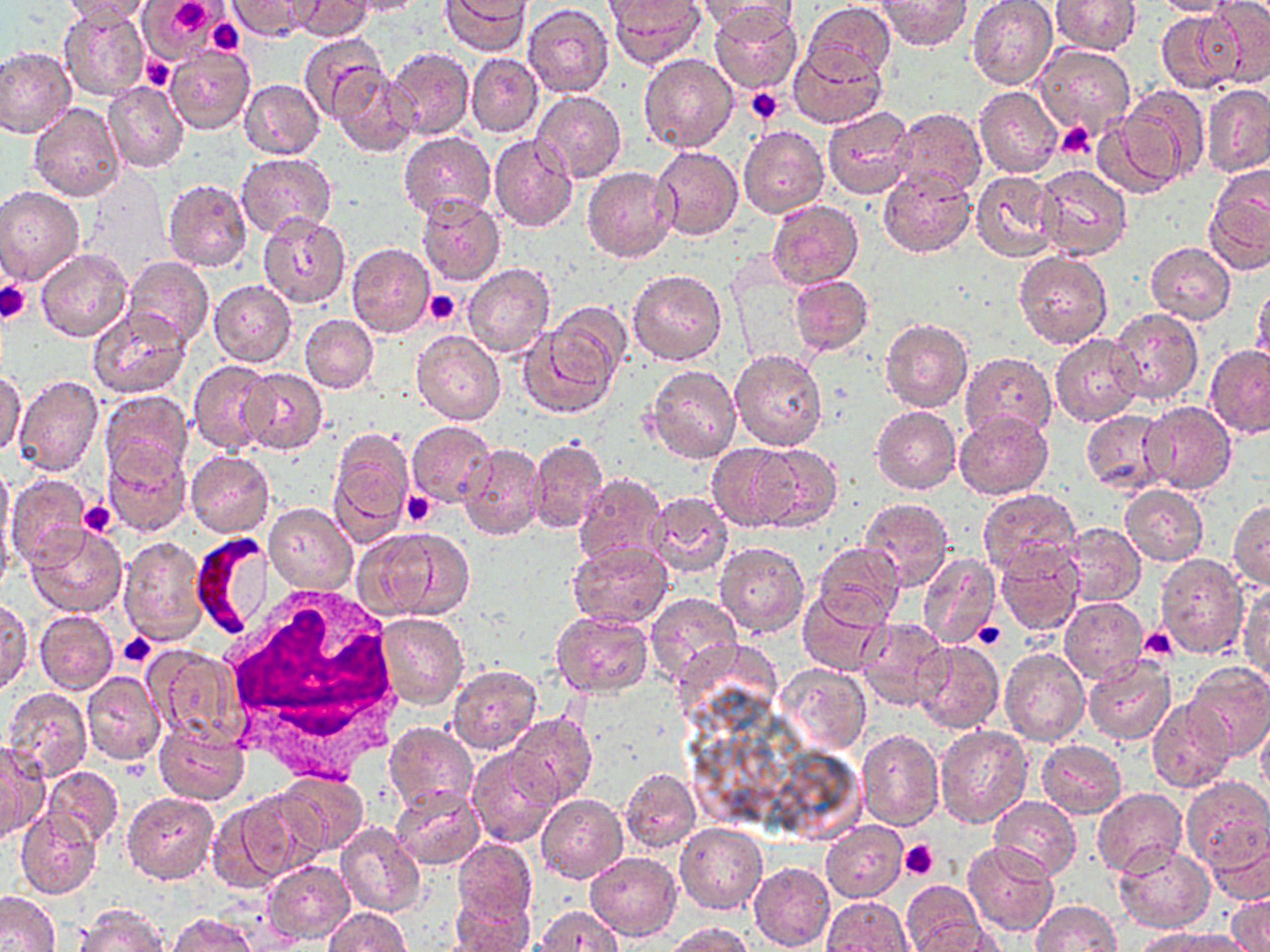

Approximate bounding boxes as (x1, y1, x2, y2) in pixels. Plasmodium falciparum-infected red blood cell locations: (191, 534, 273, 639). Platelet locations: (163, 0, 218, 38), (207, 18, 247, 55), (140, 58, 173, 90), (747, 88, 784, 124), (1055, 122, 1096, 159), (0, 279, 31, 323), (423, 290, 460, 325), (401, 491, 436, 528), (78, 501, 118, 537), (973, 622, 1003, 651), (1137, 628, 1178, 664), (117, 633, 157, 668), (899, 839, 939, 881). Uninfected red blood cell locations: (59, 0, 155, 24), (138, 0, 222, 60), (293, 0, 372, 41), (342, 0, 425, 17), (442, 0, 530, 56), (697, 0, 800, 39), (967, 0, 1057, 88), (1050, 0, 1142, 55), (1152, 0, 1240, 17), (1204, 0, 1270, 86), (230, 1, 310, 40), (607, 1, 707, 68), (877, 1, 973, 51), (805, 2, 897, 85), (522, 5, 614, 98), (709, 5, 803, 93), (58, 6, 148, 98), (1156, 8, 1244, 94), (296, 33, 389, 122), (1034, 44, 1135, 139), (0, 45, 76, 137), (166, 45, 255, 136), (787, 45, 886, 129), (387, 47, 474, 139), (466, 52, 543, 137), (639, 53, 740, 153), (333, 66, 418, 157), (239, 78, 325, 160), (103, 81, 188, 173), (1200, 84, 1270, 177), (974, 85, 1063, 177), (1119, 85, 1208, 182), (532, 90, 626, 184), (896, 99, 1067, 189), (28, 103, 123, 202), (822, 106, 914, 200), (892, 107, 987, 199), (1092, 116, 1186, 200), (739, 125, 829, 217), (399, 131, 495, 223), (488, 134, 578, 232), (653, 146, 744, 240), (236, 151, 336, 237), (1034, 163, 1131, 261), (582, 166, 676, 262), (878, 168, 976, 257), (971, 169, 1062, 262), (163, 178, 252, 272), (0, 184, 84, 285), (1204, 186, 1270, 276), (417, 195, 505, 285), (767, 199, 863, 289), (257, 212, 353, 309), (1146, 242, 1236, 324), (346, 244, 436, 338), (35, 249, 132, 342), (1014, 250, 1113, 349), (123, 258, 214, 350), (464, 263, 555, 359), (627, 269, 726, 366), (789, 275, 873, 354), (208, 279, 296, 366), (1251, 283, 1270, 374), (546, 303, 632, 388), (85, 306, 191, 399), (1109, 307, 1203, 407), (300, 314, 378, 393), (880, 318, 972, 413), (517, 324, 619, 420), (411, 329, 505, 424), (1050, 334, 1143, 426), (1205, 345, 1270, 436), (729, 349, 828, 451), (960, 352, 1057, 442), (188, 359, 276, 454), (646, 366, 742, 464), (238, 367, 328, 454), (1, 370, 27, 456), (13, 373, 103, 477), (100, 389, 193, 485), (1140, 401, 1236, 494), (871, 405, 961, 494), (1083, 409, 1174, 493), (954, 410, 1054, 500), (407, 421, 496, 506), (328, 427, 415, 538), (528, 438, 609, 534), (102, 443, 191, 536), (457, 443, 545, 541), (706, 443, 804, 530), (747, 444, 842, 532), (186, 451, 274, 537), (0, 464, 14, 554), (574, 473, 667, 571), (6, 475, 93, 568), (1119, 484, 1208, 566), (976, 487, 1080, 578), (647, 492, 734, 576), (860, 497, 954, 589), (1229, 499, 1269, 590), (263, 502, 355, 594), (1061, 522, 1146, 607), (27, 525, 127, 616), (356, 531, 468, 622), (119, 536, 208, 645), (714, 541, 810, 637), (814, 541, 905, 627), (568, 543, 674, 628), (993, 546, 1084, 636), (917, 553, 1001, 650), (1153, 554, 1250, 660), (1240, 585, 1268, 684), (797, 589, 890, 676), (645, 592, 742, 686), (1060, 596, 1148, 683), (1, 600, 32, 691), (33, 610, 120, 695), (549, 611, 654, 697), (376, 612, 468, 707), (857, 618, 952, 710), (913, 641, 1004, 734), (142, 644, 244, 744), (999, 647, 1090, 747), (1083, 656, 1174, 744), (1185, 661, 1270, 760), (775, 663, 872, 756), (447, 665, 543, 755), (81, 671, 165, 766), (4, 687, 92, 781), (1147, 701, 1235, 792), (506, 713, 597, 806), (1256, 718, 1270, 796), (153, 721, 250, 804), (384, 722, 478, 814), (934, 724, 1032, 828), (857, 730, 943, 830), (1036, 739, 1126, 817), (0, 740, 46, 843), (469, 747, 562, 849), (43, 765, 124, 847), (619, 768, 701, 855), (274, 770, 367, 854), (1181, 777, 1270, 873), (390, 786, 486, 869), (1092, 788, 1186, 878), (236, 790, 329, 881), (121, 792, 219, 884), (537, 793, 627, 882), (989, 796, 1081, 881), (208, 800, 296, 893), (16, 809, 100, 897), (335, 821, 428, 917), (675, 822, 767, 913), (820, 822, 907, 903), (1204, 822, 1270, 906), (455, 839, 538, 927), (963, 840, 1058, 936), (1114, 844, 1215, 931), (585, 850, 681, 940), (263, 860, 354, 945), (749, 862, 835, 950), (901, 882, 986, 951), (0, 891, 60, 951), (449, 893, 533, 952), (1228, 893, 1270, 952), (820, 897, 911, 951), (1030, 900, 1121, 951), (74, 905, 168, 952), (535, 906, 625, 950), (323, 907, 411, 952), (167, 913, 257, 951), (906, 919, 1005, 952), (665, 923, 754, 952), (1134, 928, 1234, 952). White blood cell locations: (222, 581, 406, 776). Slide-level diagnosis: Plasmodium falciparum. Optical microscopy. Thin blood film. Single field of view. Captured at 1000x magnification. Image is 1270×952 pixels. May-Grünwald-Giemsa-stained preparation.